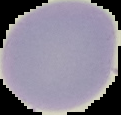

Summary:
  - Preparation: thin blood smear
  - Image size: 121×115 pixels
  - Malaria status: uninfected
  - Image type: segmented cell region with the area outside set to black